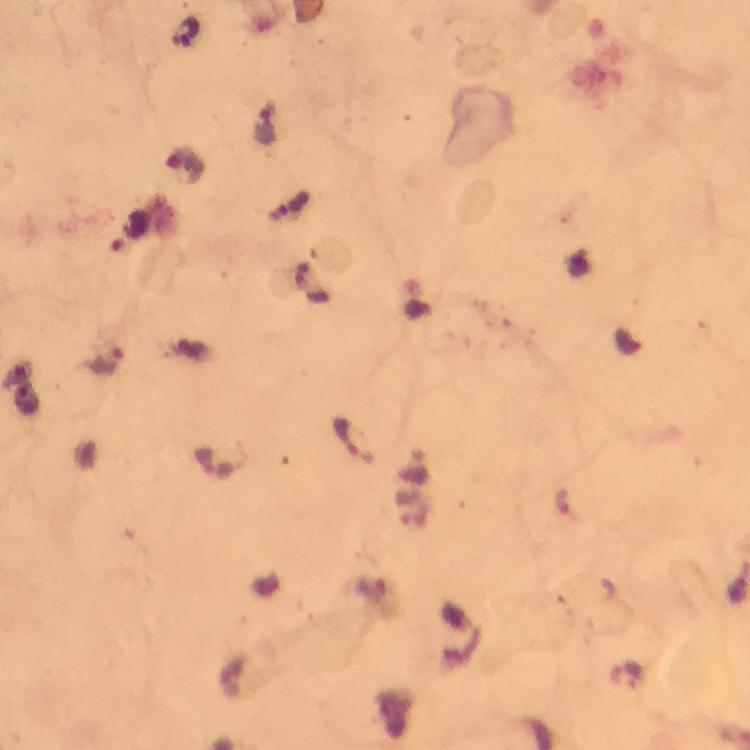
Approximate centers as {x, y} in pixels. Malaria parasite locations: {185, 33}, {267, 123}, {187, 165}, {130, 232}, {108, 362}, {355, 440}. Image is 750×750 pixels. Photographed with a smartphone mounted on the microscope. From a malaria diagnostic workup. Cropped region of a single field of view. Giemsa stain. Immersion oil applied. 100x magnification. Thick smear.